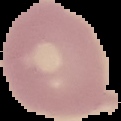

From a thin blood smear. Image is 121×121 pixels. Malaria status: uninfected. Segmented cell region on a black background.